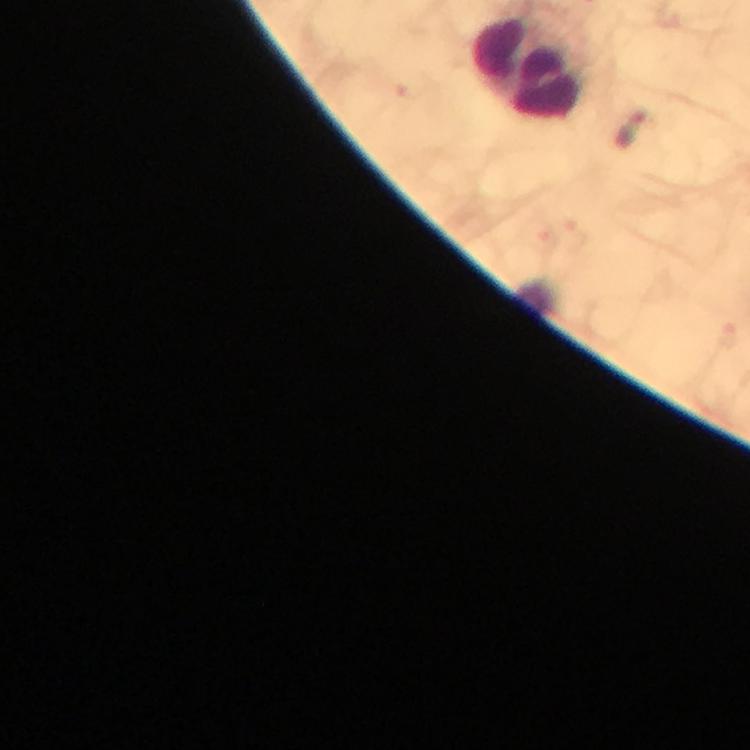
context: from a malaria diagnostic workup
cropped_from: a single field of view
stain: Giemsa
leukocyte_locations: 'approximate object centers, in pixels from the top-left corner: (x=529, y=67)'
capture: smartphone camera through the microscope
malaria_parasite_locations: 'approximate object centers, in pixels from the top-left corner: (x=632, y=131)'
immersion_oil: used
image_size: 750×750 pixels
magnification: 100x
preparation: thick blood film